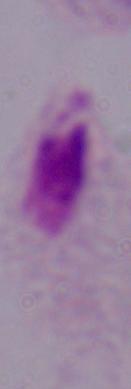

magnification = 1000x
modality = photomicrograph
identification = trichomonad